Give the extent of all Trypanosoma brucei.
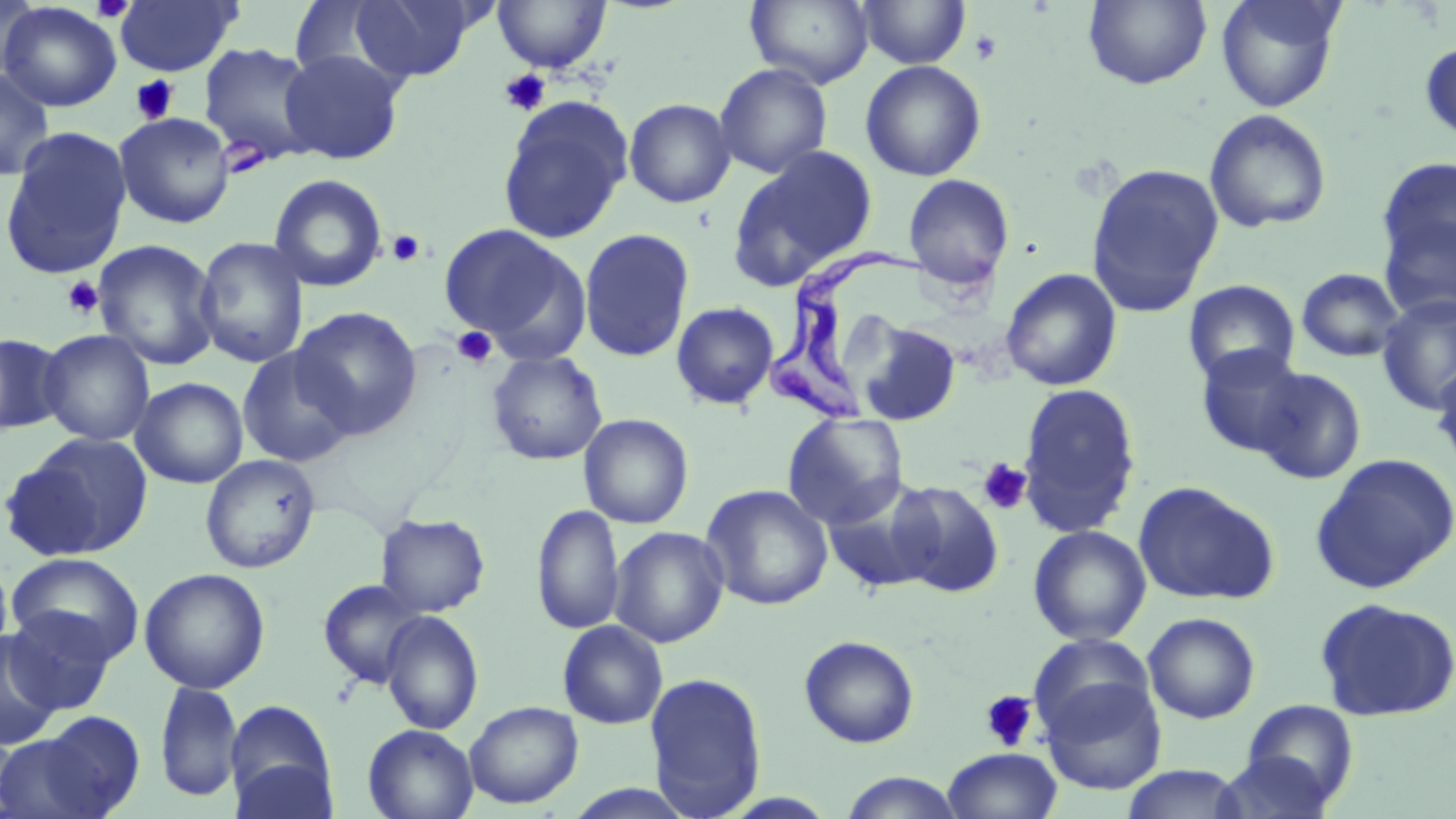

Approximate bounding boxes as (x1, y1, x2, y2) in pixels.
Trypanosoma brucei: (764, 245, 929, 424).

Summary:
  - Platelet locations: (91, 0, 135, 23), (969, 29, 1002, 64), (498, 68, 551, 116), (130, 75, 180, 125), (387, 230, 425, 267), (62, 276, 104, 319), (451, 326, 498, 368), (977, 457, 1032, 514), (980, 690, 1039, 751)
  - Uninfected red blood cell locations: (0, 0, 39, 83), (347, 0, 478, 83), (745, 0, 874, 88), (857, 0, 971, 69), (1083, 0, 1212, 90), (1214, 0, 1346, 112), (113, 1, 242, 77), (492, 1, 611, 74), (0, 2, 122, 112), (287, 2, 406, 84), (1419, 40, 1456, 145), (198, 42, 321, 165), (279, 48, 407, 164), (859, 59, 987, 181), (714, 62, 833, 178), (0, 67, 56, 182), (497, 97, 633, 244), (624, 98, 736, 208), (1204, 108, 1332, 233), (114, 112, 235, 228), (0, 126, 133, 280), (728, 145, 877, 290), (1374, 155, 1455, 305), (1086, 162, 1224, 315), (269, 173, 388, 292), (902, 173, 1015, 292), (438, 222, 586, 355), (578, 227, 695, 363), (193, 236, 309, 368), (92, 239, 222, 371), (1296, 267, 1406, 362), (1001, 268, 1122, 391), (1182, 279, 1300, 386), (1376, 295, 1456, 414), (671, 302, 780, 410), (291, 306, 423, 439), (852, 318, 961, 427), (38, 329, 155, 446), (0, 332, 68, 435), (1194, 344, 1307, 457), (236, 345, 357, 469), (487, 351, 608, 465), (1431, 361, 1456, 476), (1253, 367, 1367, 484), (131, 377, 248, 488), (1017, 382, 1142, 537), (782, 412, 909, 529), (578, 413, 693, 529), (4, 432, 154, 561), (1311, 452, 1456, 594), (200, 454, 321, 573), (821, 479, 939, 593), (887, 480, 1006, 598), (1132, 480, 1280, 606), (700, 484, 834, 611), (531, 503, 625, 635), (375, 513, 491, 618), (1028, 525, 1151, 645), (609, 526, 729, 648), (0, 550, 14, 666), (6, 553, 144, 665), (139, 567, 271, 694), (317, 578, 427, 689), (1314, 596, 1456, 723), (3, 607, 117, 714), (379, 610, 484, 735), (1142, 612, 1261, 724), (557, 620, 668, 730), (0, 630, 63, 750), (1028, 632, 1155, 742), (799, 635, 920, 749), (644, 671, 768, 817), (1041, 679, 1167, 794), (154, 681, 242, 803), (225, 699, 338, 817), (1239, 699, 1360, 808), (465, 701, 583, 809), (31, 711, 145, 817), (362, 723, 479, 819), (0, 727, 23, 817), (0, 732, 105, 819), (942, 747, 1062, 819), (1214, 752, 1337, 819), (1119, 765, 1248, 819), (838, 771, 966, 818), (562, 784, 701, 819)
  - Slide-level diagnosis: Trypanosoma brucei
  - Stain: May-Grünwald-Giemsa
  - Magnification: 1000x
  - Image size: 1456×819 pixels
  - Preparation: thin blood smear
  - Field of view: single
  - Modality: optical microscopy